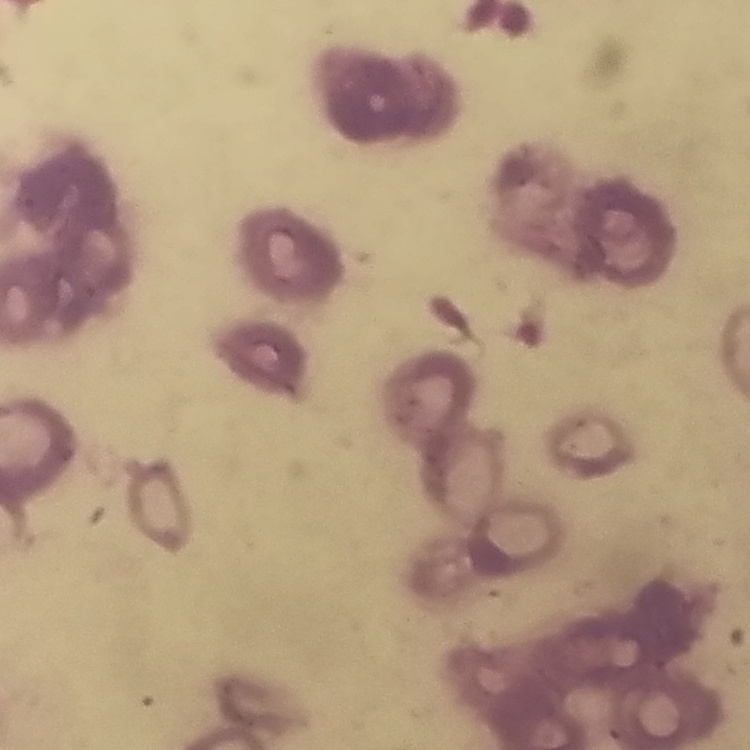

Summary:
  - Red blood cell morphology: rouleaux formation
  - Stain: Field's or Giemsa
  - Preparation: thin blood film
  - Image type: one tile cut from a larger photomicrograph